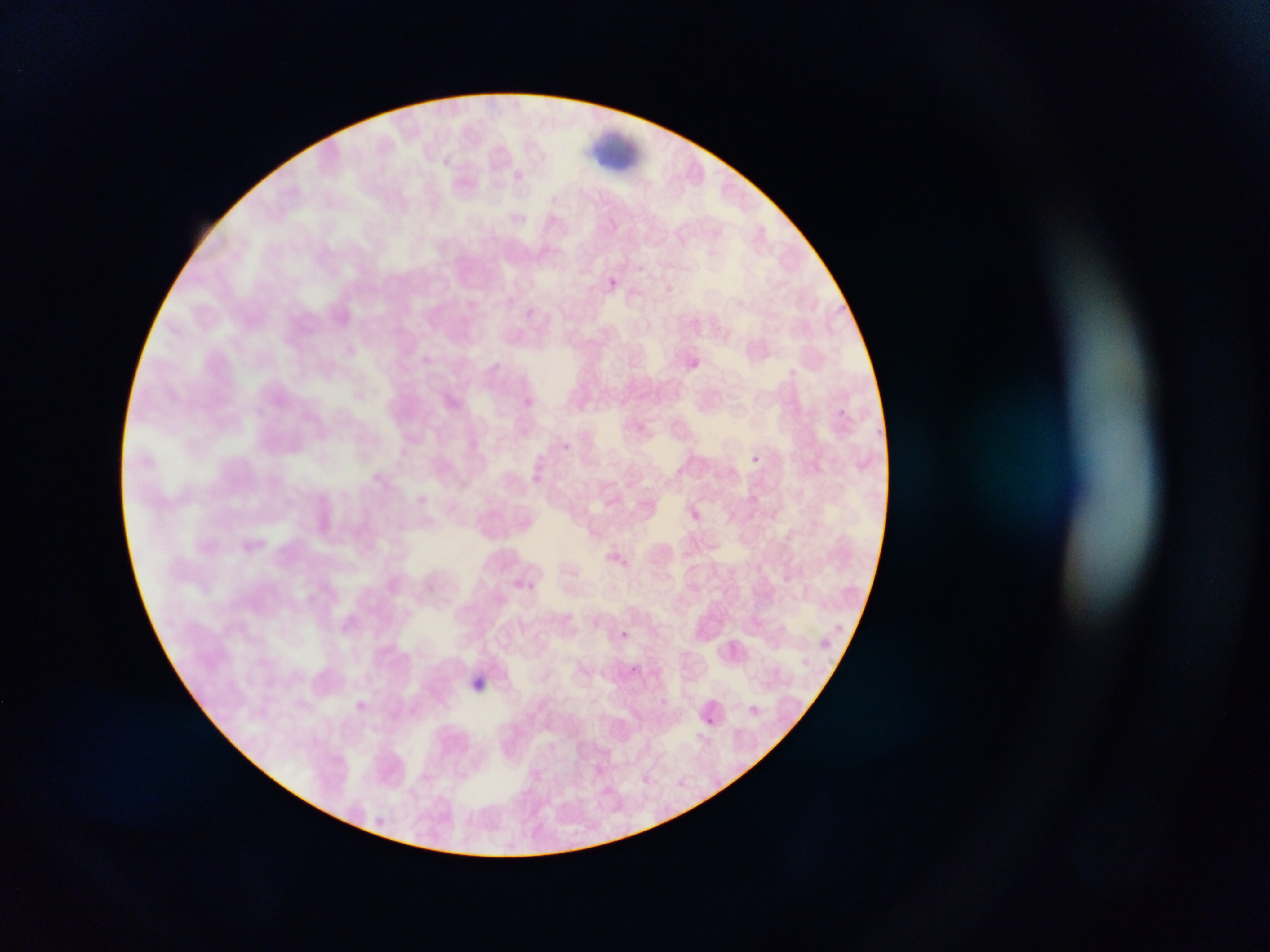

Approximate bounding boxes as (left, top, right, bottom) in pixels. Plasmodium parasite locations: (607, 270, 623, 297), (559, 437, 576, 454), (751, 453, 768, 466), (619, 627, 631, 640), (628, 663, 644, 682), (350, 697, 367, 713), (704, 715, 715, 727) | approximate (x, y) pixel centers of objects too small to bound: (839, 411). Leukocyte locations: (582, 117, 641, 172). Thin blood film. Image is 1270×952 pixels. Photographed through a microscope with a mobile-phone camera. One field of view. Collected in Ghana.